Locate every Plasmodium vivax-infected red blood cell.
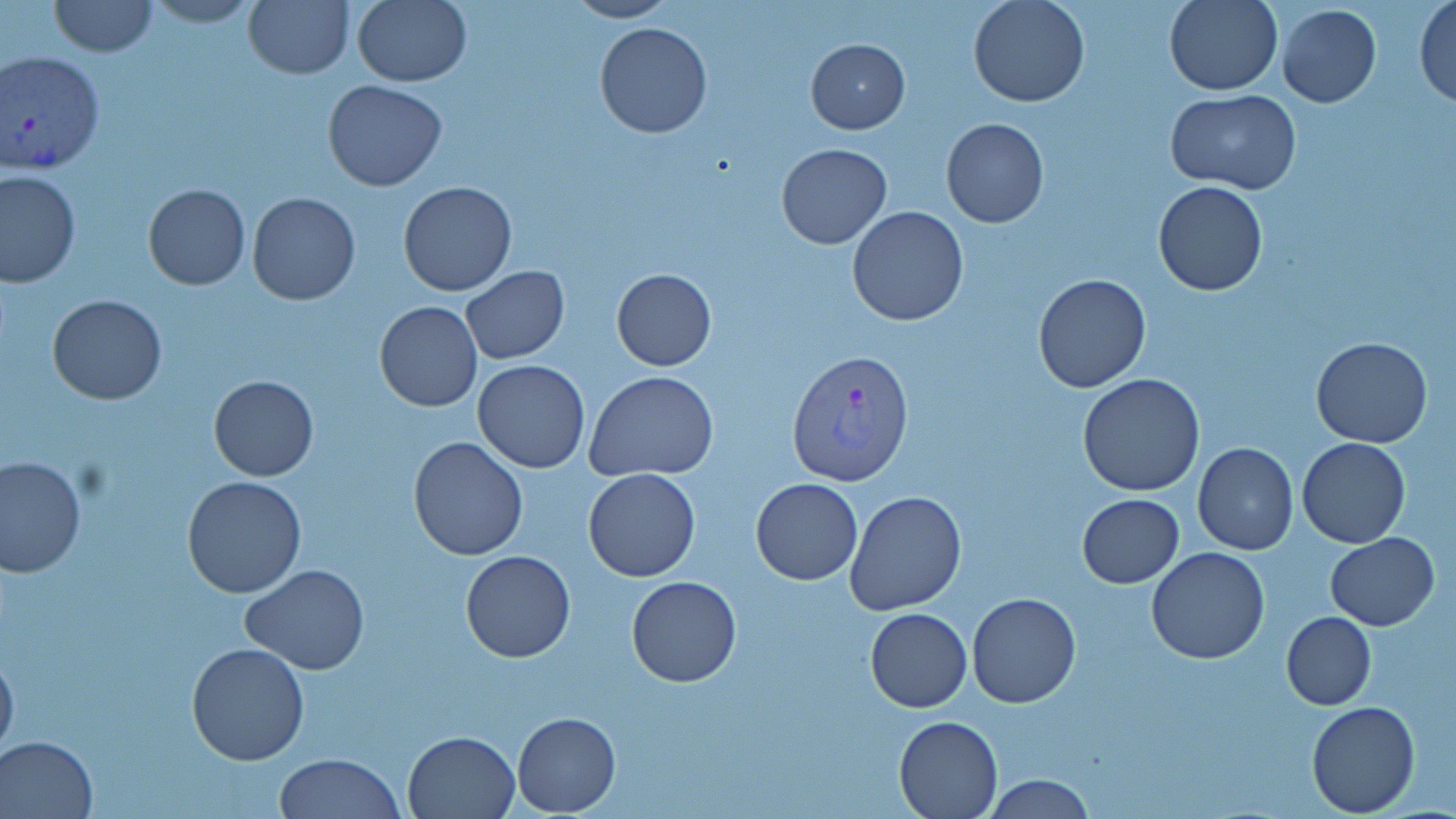
Approximate bounding boxes as (x1,y1)-(x2,y2) corner pairs in pixels.
Plasmodium vivax-infected red blood cells: (0,49)-(103,177), (787,349)-(916,487).

{
  "slide_level_diagnosis": "Plasmodium vivax",
  "uninfected_red_blood_cell_locations": "approximate bounding boxes as (x1,y1)-(x2,y2) corner pairs in pixels: (47,0)-(157,57), (141,0)-(262,27), (243,0)-(353,79), (352,0)-(472,86), (563,0)-(678,23), (969,0)-(1089,107), (1163,0)-(1283,95), (1413,1)-(1456,106), (1277,4)-(1382,108), (592,22)-(713,138), (806,38)-(909,133), (323,80)-(447,192), (1166,90)-(1300,192), (940,117)-(1049,227), (776,141)-(892,249), (0,170)-(80,286), (1153,180)-(1269,295), (398,181)-(519,297), (143,184)-(250,290), (246,192)-(361,305), (846,206)-(969,327), (461,266)-(569,364), (611,267)-(716,370), (1032,273)-(1151,393), (47,295)-(167,405), (374,301)-(483,413), (1311,336)-(1433,448), (472,360)-(591,473), (585,370)-(718,482), (1078,372)-(1204,497), (208,375)-(318,482), (425,378)-(574,538), (408,435)-(529,559), (1297,437)-(1411,548), (1192,442)-(1298,555), (0,454)-(85,577), (583,467)-(702,582), (181,475)-(306,598), (750,477)-(863,585), (843,488)-(968,615), (1078,493)-(1184,588), (1324,533)-(1440,630), (1147,548)-(1270,663), (460,550)-(575,662), (241,566)-(368,675), (627,576)-(742,687), (967,593)-(1080,708), (865,607)-(973,713), (1282,611)-(1376,711), (0,643)-(19,763), (186,643)-(310,766), (1307,700)-(1421,817), (513,712)-(621,815), (894,714)-(1003,817), (403,730)-(519,817), (0,734)-(99,818), (275,753)-(406,819), (982,773)-(1097,818)",
  "modality": "light microscopy",
  "image_size": "1456×819 pixels",
  "field_of_view": "single",
  "stain": "May-Grünwald-Giemsa",
  "preparation": "thin blood smear",
  "magnification": "1000x"
}